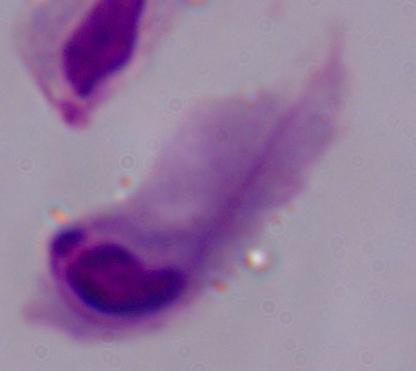 A trichomonad is shown. Photomicrograph. 1000x magnification.